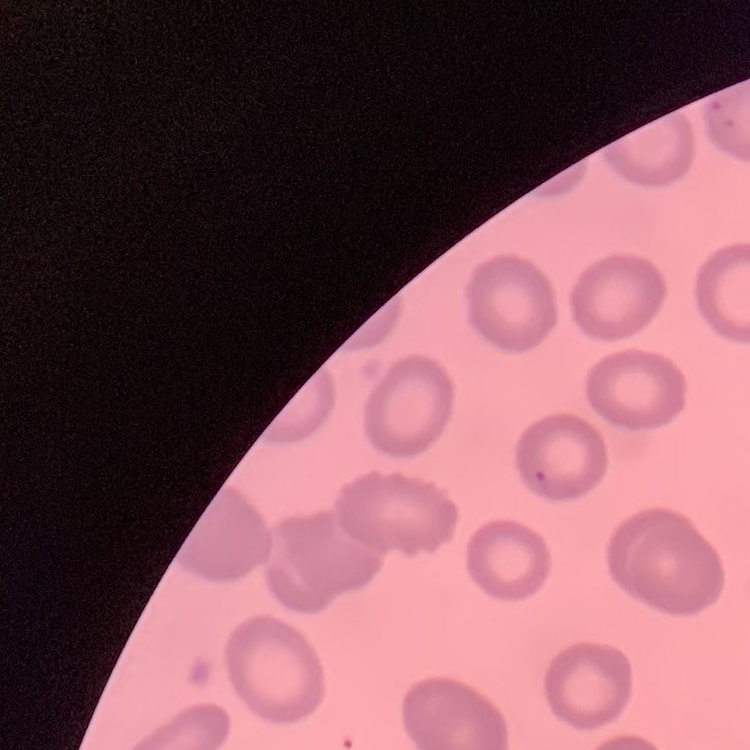

red blood cell morphology = no rouleaux formation
image type = square crop of a larger photomicrograph
preparation = thin peripheral smear
stain = Field's or Giemsa